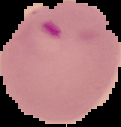
Result: Plasmodium parasites detected. Image is 121×127 pixels. Segmented cell region on a black background. From a thin blood film.